Locate every Plasmodium parasite.
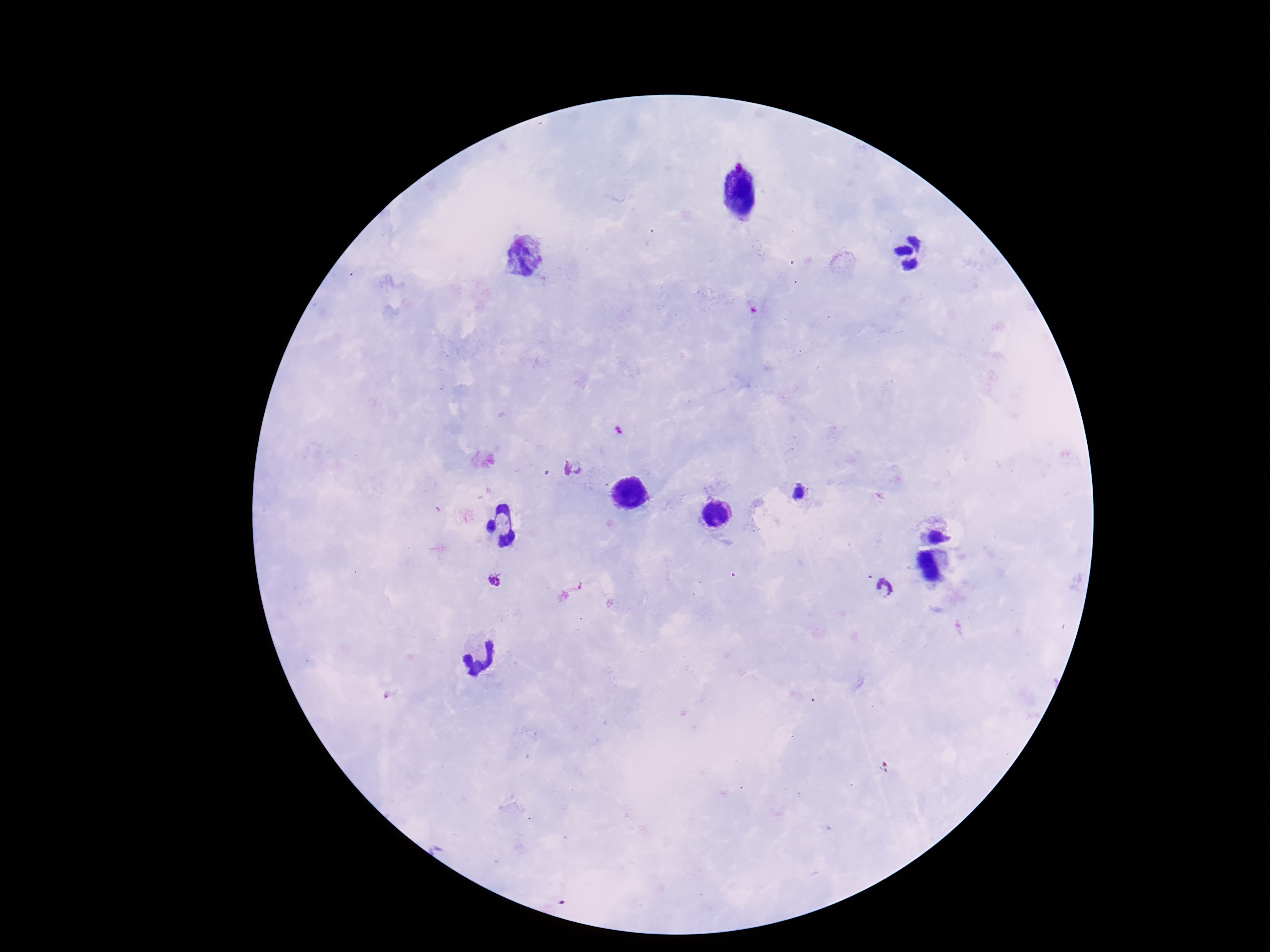
Approximate centers as {x, y} in pixels.
Plasmodium parasites: {572, 468}, {495, 581}, {883, 588}.

Image is 1270×952 pixels. 100x magnification. Thick blood film. Giemsa stain. Patient malaria status: infected. Single field of view. Smartphone photograph taken through the microscope eyepiece.